Identify the parasite.
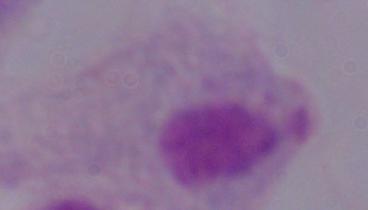
This is a trichomonad.

modality = photomicrograph
magnification = 1000x